Name the parasite shown.
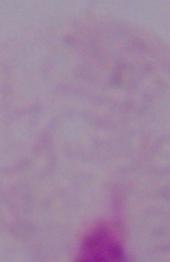
This is a trichomonad.

magnification = 1000x
modality = photomicrograph